State which parasite is depicted.
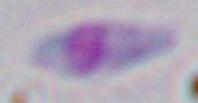
This is Toxoplasma gondii.

modality = micrograph
magnification = 1000x